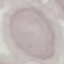

{
  "result": "no malaria parasites detected",
  "stain": "Giemsa",
  "image_type": "cell patch, automatically extracted from a larger field of view and resized to 64 × 64 pixels",
  "preparation": "thin smear",
  "capture": "smartphone through the microscope eyepiece"
}